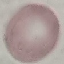

Summary:
  - Result: no malaria parasites detected
  - Stain: Giemsa
  - Preparation: thin blood smear
  - Image type: cell patch, automatically extracted from a larger field of view and resized to 64 × 64 pixels
  - Capture: smartphone camera at the microscope eyepiece